Give the extent of all Plasmodium parasites.
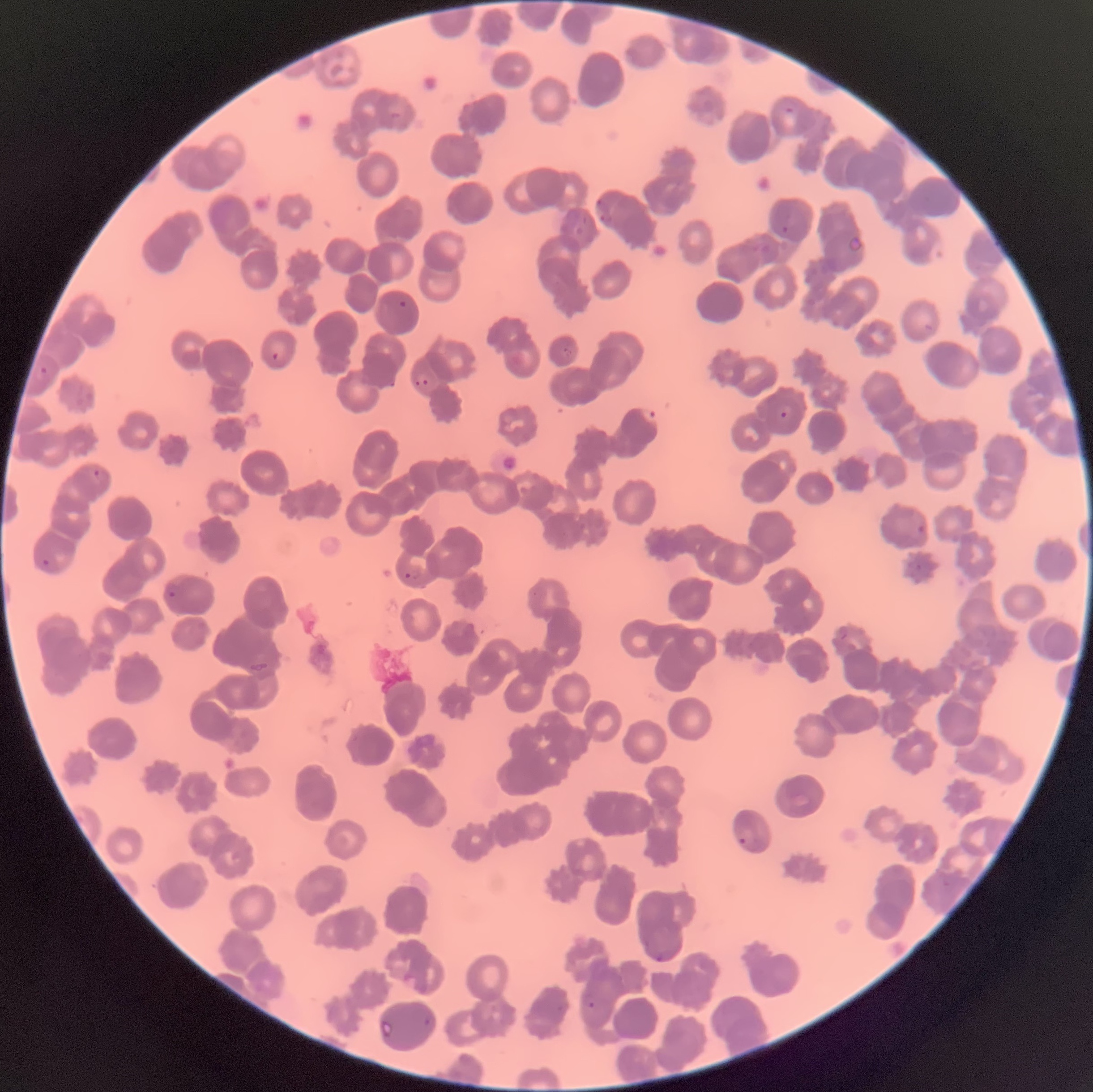
Approximate bounding boxes as (x1,y1)-(x2,y2) corner pairs in pixels.
Plasmodium parasites: (782,105)-(796,115), (389,111)-(403,120), (596,199)-(610,212), (600,212)-(613,225), (779,224)-(790,235), (849,235)-(864,254), (397,299)-(408,309), (923,323)-(934,332), (562,347)-(574,357), (269,351)-(280,361), (39,366)-(47,375), (414,373)-(430,387), (388,380)-(396,388), (780,404)-(793,419), (640,405)-(660,426), (93,468)-(101,479), (916,524)-(925,532), (42,559)-(51,566), (404,571)-(417,580), (166,589)-(177,598), (839,628)-(850,642), (249,662)-(270,673), (738,829)-(753,845), (656,950)-(674,963), (581,991)-(595,1010), (424,1017)-(431,1026).

Light microscopy. Thin blood smear. Image is 1093×1092 pixels. The red blood cells show rouleaux formation.